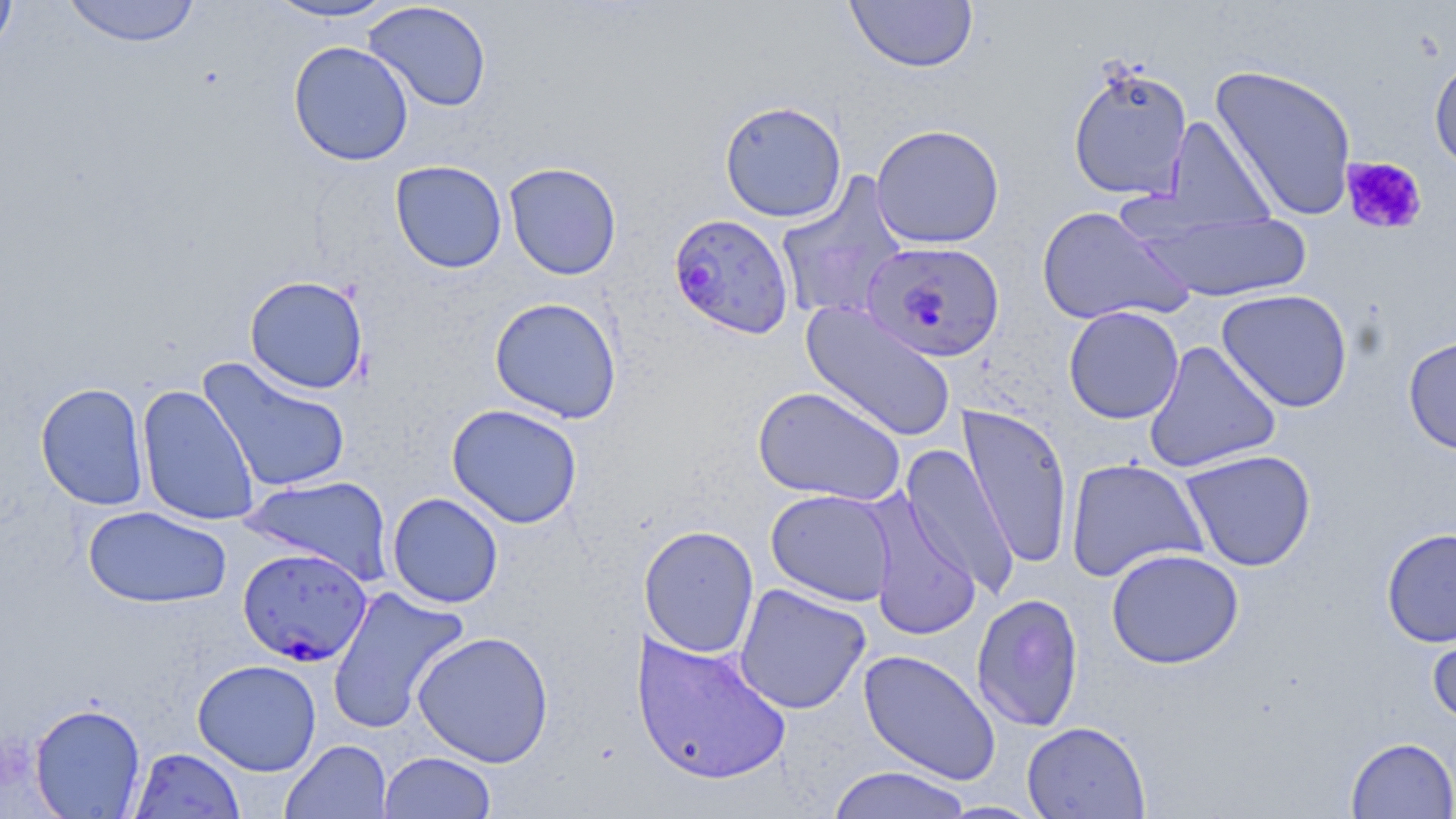 Approximate bounding boxes as (x1,y1)-(x2,y2) corner pairs in pixels. Uninfected red blood cell locations: (0,0)-(18,58), (62,0)-(202,47), (262,0)-(402,22), (845,1)-(978,72), (364,2)-(492,112), (288,41)-(414,166), (1429,52)-(1456,175), (1067,61)-(1194,202), (1209,63)-(1358,222), (719,100)-(847,223), (1162,115)-(1276,232), (870,123)-(1005,249), (390,160)-(507,273), (504,162)-(622,280), (775,173)-(909,323), (1036,205)-(1195,327), (1134,208)-(1313,303), (244,275)-(369,394), (1216,288)-(1354,413), (489,296)-(623,423), (801,301)-(957,441), (1063,305)-(1185,424), (1403,333)-(1456,455), (1143,340)-(1282,473), (197,356)-(351,494), (35,381)-(150,510), (136,384)-(260,527), (752,385)-(906,506), (446,403)-(583,528), (958,403)-(1074,570), (900,444)-(1020,598), (1179,449)-(1317,571), (1065,458)-(1209,584), (242,475)-(393,584), (765,489)-(897,607), (387,492)-(504,608), (863,492)-(982,641), (83,506)-(232,608), (639,525)-(760,659), (1381,527)-(1456,647), (1105,548)-(1244,669), (733,583)-(872,715), (327,584)-(470,734), (971,592)-(1084,732), (1426,611)-(1456,727), (412,630)-(555,768), (630,632)-(792,785), (858,649)-(1001,785), (192,659)-(322,776), (29,702)-(146,818), (1021,720)-(1151,819), (1346,736)-(1456,818), (280,739)-(393,819), (129,747)-(246,818), (378,751)-(497,818), (826,765)-(974,818), (936,800)-(1049,818). Platelet locations: (1341,156)-(1427,235). Plasmodium falciparum-infected red blood cell locations: (668,213)-(795,339), (860,240)-(1005,362), (237,547)-(373,667). Slide-level diagnosis: Plasmodium falciparum. May-Grünwald-Giemsa stain. Thin blood film. 1000x magnification. Single field of view. Optical microscopy. Image is 1456×819 pixels.